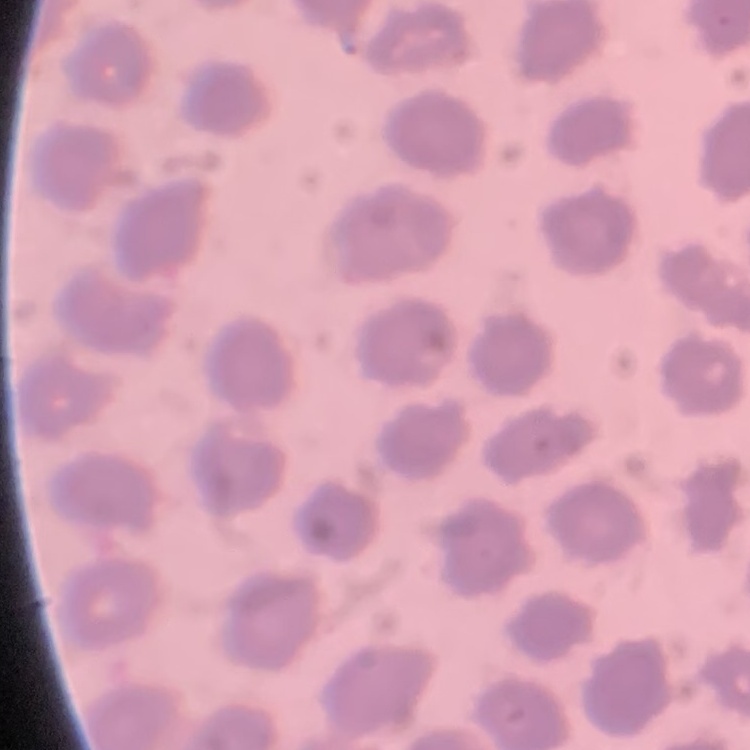
erythrocyte morphology = no rouleaux formation
preparation = thin blood smear
image type = one tile cut from a larger photomicrograph
stain = Field's or Giemsa